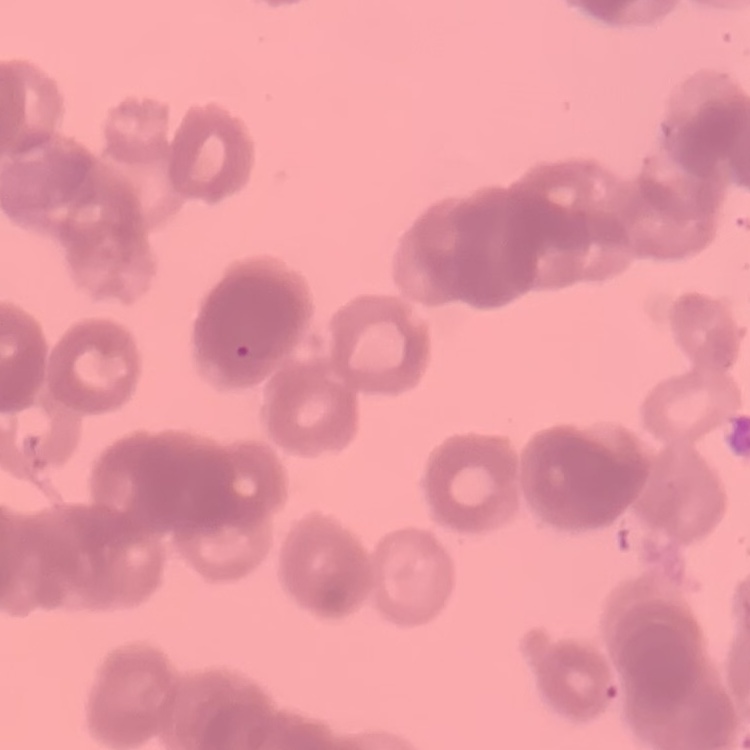

The erythrocytes show rouleaux formation. Field's or Giemsa stain. Thin blood film. One tile cut from a larger photomicrograph.